Locate cells.
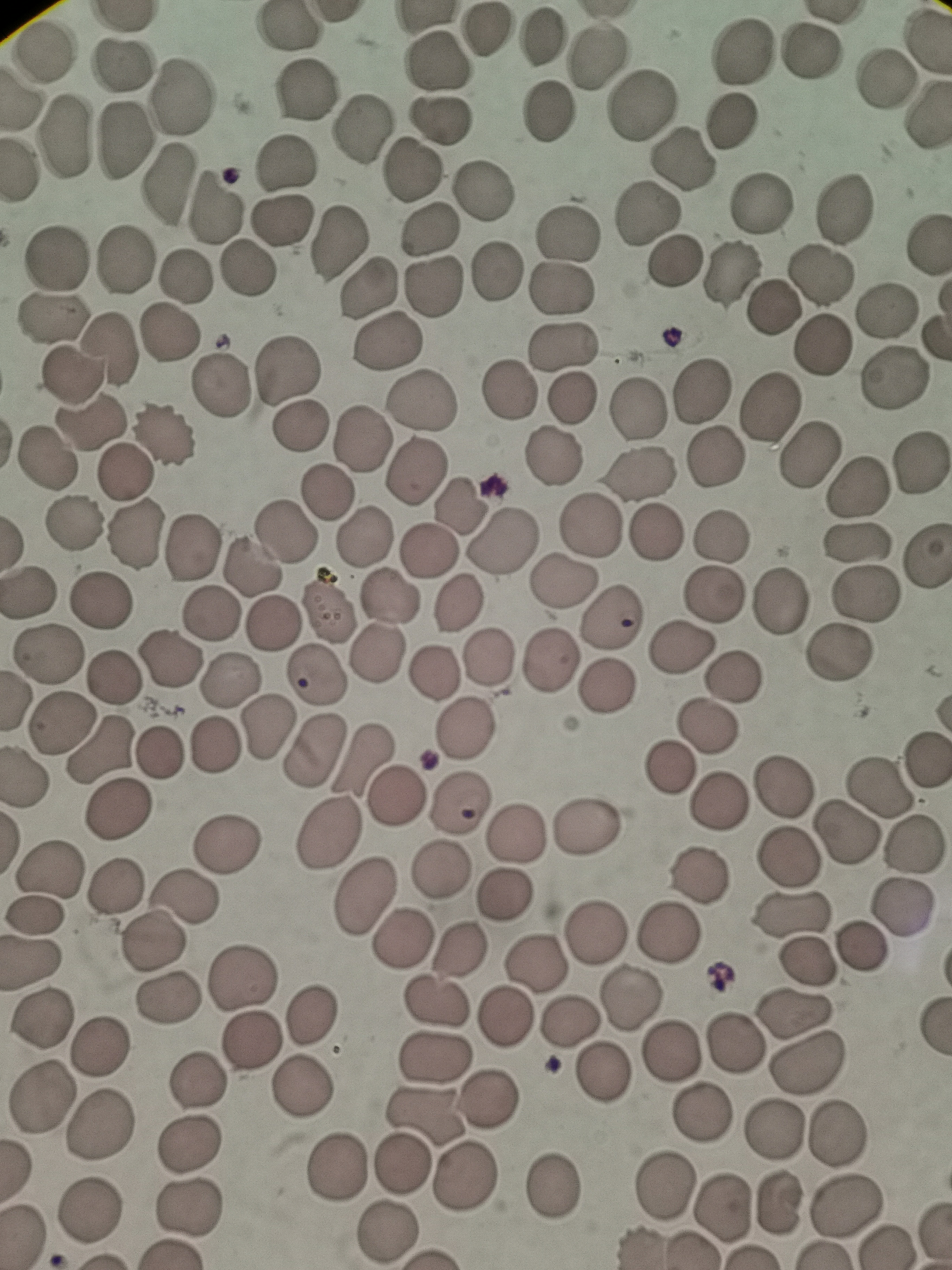
Approximate centers as (x, y) in pixels.
Cells: (284, 29), (481, 33), (540, 38), (810, 52), (39, 53), (744, 53), (597, 55), (123, 62), (440, 62), (888, 80), (304, 90), (179, 99), (638, 108), (548, 112), (439, 120), (732, 120), (361, 129), (62, 136), (124, 138), (684, 158), (411, 172), (167, 183), (482, 191), (761, 202), (839, 209), (215, 211), (648, 214), (280, 220), (424, 229), (568, 232), (337, 244), (56, 260), (675, 261), (242, 269), (495, 272), (729, 273), (820, 273), (183, 276), (432, 285), (367, 288), (558, 288), (772, 308), (885, 309), (52, 318), (169, 333), (390, 341), (820, 344), (560, 346), (105, 350), (286, 372), (75, 378), (892, 379), (219, 386), (511, 390), (702, 392), (572, 397), (420, 400), (768, 405), (636, 409), (87, 420), (299, 426), (163, 434), (363, 439), (811, 454), (716, 456), (46, 458), (553, 458), (919, 464), (125, 472), (639, 473), (413, 474), (856, 482), (326, 495), (459, 502), (72, 525), (591, 525), (656, 530), (283, 531), (132, 532), (721, 537), (361, 538), (855, 539), (506, 544), (190, 547), (426, 549), (249, 569), (563, 582), (27, 592), (712, 593), (867, 595), (386, 597), (782, 600), (96, 601), (456, 605), (327, 607), (213, 614), (611, 618), (270, 623), (677, 647), (49, 652), (839, 652), (375, 654), (490, 654), (550, 658), (172, 662), (317, 672), (435, 676), (114, 677), (730, 677), (228, 678), (606, 686), (59, 725), (465, 725), (267, 727), (704, 728), (217, 742), (311, 747), (102, 751), (160, 753), (362, 756), (925, 761), (669, 764), (24, 776), (784, 787), (880, 788), (395, 797), (719, 800), (461, 804), (119, 809), (586, 825), (327, 831), (516, 831), (844, 831), (231, 843), (911, 844), (787, 860), (52, 867), (440, 868), (700, 876), (113, 888), (367, 893), (506, 894), (185, 895), (901, 903), (795, 916), (34, 919), (401, 933), (596, 935), (671, 935), (150, 943), (458, 946), (857, 949), (31, 962), (807, 963), (534, 966), (242, 974), (170, 997), (436, 1000), (630, 1001), (796, 1013), (313, 1018), (503, 1018), (40, 1019), (571, 1022), (735, 1040), (252, 1042), (98, 1043), (670, 1047), (434, 1058), (807, 1061), (602, 1073), (202, 1082), (305, 1085), (39, 1094), (490, 1098), (702, 1110), (426, 1115), (101, 1122), (774, 1129), (837, 1133), (190, 1141), (402, 1166), (337, 1167), (465, 1175), (554, 1187), (663, 1188), (779, 1203), (724, 1206), (845, 1206), (93, 1207), (187, 1207), (386, 1231).

Giemsa-stained preparation. Thin blood smear. Image is 952×1270 pixels. Photographed with a smartphone camera at the microscope eyepiece. Single field of view.